Identify the parasite.
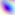
This is Toxoplasma gondii.

Micrograph. 400x magnification.